Classify this cell by malaria status.
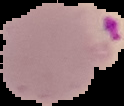
It is parasitized.

image_type: segmented cell region on a black background
preparation: thin blood smear
image_size: 124×106 pixels